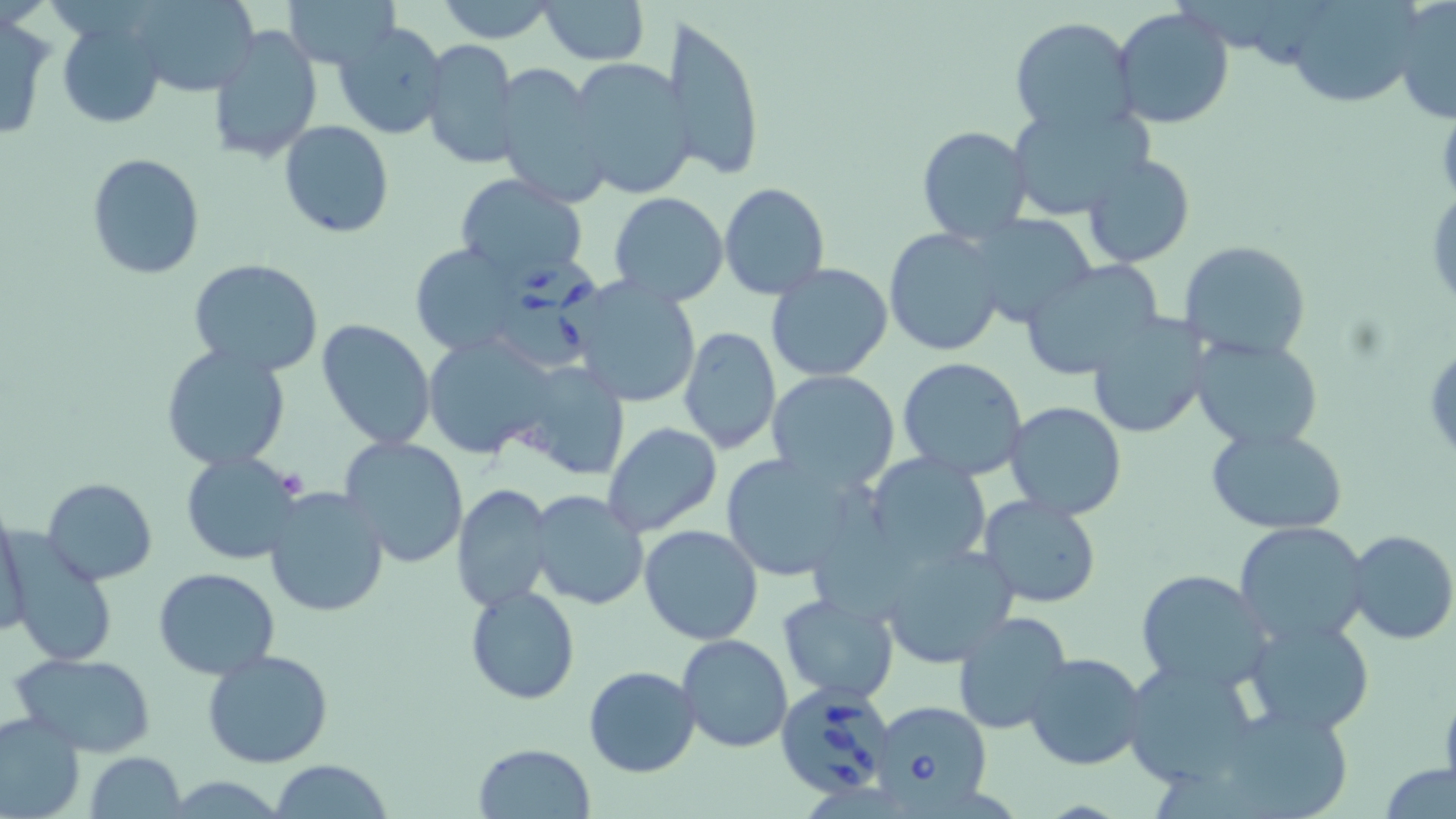 Approximate bounding boxes as (x1, y1, x2, y2) in pixels. Uninfected red blood cell locations: (130, 0, 262, 95), (282, 0, 398, 68), (536, 0, 652, 67), (1391, 0, 1455, 125), (434, 1, 560, 43), (1280, 1, 1427, 107), (1113, 6, 1236, 130), (666, 12, 766, 182), (0, 13, 52, 142), (59, 15, 166, 129), (1010, 17, 1138, 136), (333, 20, 450, 143), (208, 24, 323, 164), (422, 38, 520, 171), (565, 57, 695, 200), (496, 61, 610, 208), (1007, 102, 1152, 223), (279, 120, 395, 237), (916, 126, 1032, 244), (85, 153, 205, 281), (1081, 154, 1195, 269), (454, 174, 589, 286), (718, 182, 830, 299), (608, 192, 729, 307), (965, 214, 1098, 329), (883, 227, 1006, 359), (1177, 239, 1312, 363), (410, 244, 526, 356), (188, 257, 324, 376), (1019, 258, 1164, 380), (765, 263, 895, 383), (561, 277, 703, 412), (1086, 313, 1211, 440), (317, 319, 436, 448), (677, 326, 782, 454), (421, 330, 559, 458), (1190, 336, 1324, 453), (159, 345, 293, 470), (897, 357, 1029, 481), (509, 361, 630, 482), (766, 370, 901, 493), (1004, 401, 1128, 519), (602, 421, 723, 537), (1205, 424, 1349, 534), (340, 436, 470, 568), (718, 450, 870, 583), (180, 451, 307, 564), (865, 454, 994, 569), (42, 477, 157, 586), (452, 484, 554, 612), (262, 485, 390, 618), (527, 489, 650, 611), (976, 493, 1106, 609), (0, 507, 29, 638), (1234, 521, 1370, 646), (639, 525, 763, 644), (1343, 529, 1456, 646), (6, 538, 116, 665), (881, 540, 1019, 670), (152, 567, 279, 679), (1135, 568, 1277, 692), (464, 585, 580, 703), (777, 593, 899, 704), (951, 611, 1074, 735), (1242, 616, 1377, 739), (677, 633, 793, 752), (203, 648, 333, 768), (12, 651, 156, 756), (1023, 651, 1148, 772), (1121, 658, 1263, 790), (583, 665, 700, 778), (0, 709, 85, 819), (474, 742, 596, 818), (85, 751, 187, 818), (272, 759, 393, 818), (1379, 761, 1456, 817). Babesia divergens-infected red blood cell locations: (500, 255, 613, 364), (775, 680, 899, 801), (868, 700, 994, 810). Slide-level diagnosis: Babesia divergens. Image is 1456×819 pixels. Single field of view. 1000x magnification. Optical microscopy. Thin blood film. May-Grünwald-Giemsa-stained preparation.